Name the parasite shown.
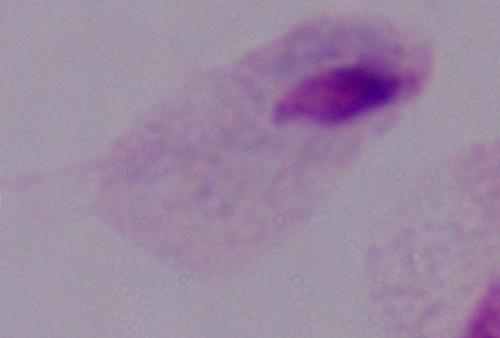
A trichomonad.

magnification: 1000x
modality: photomicrograph